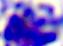
Summary:
  - Identification: white blood cell
  - Magnification: 400x
  - Modality: micrograph